Report the malaria status.
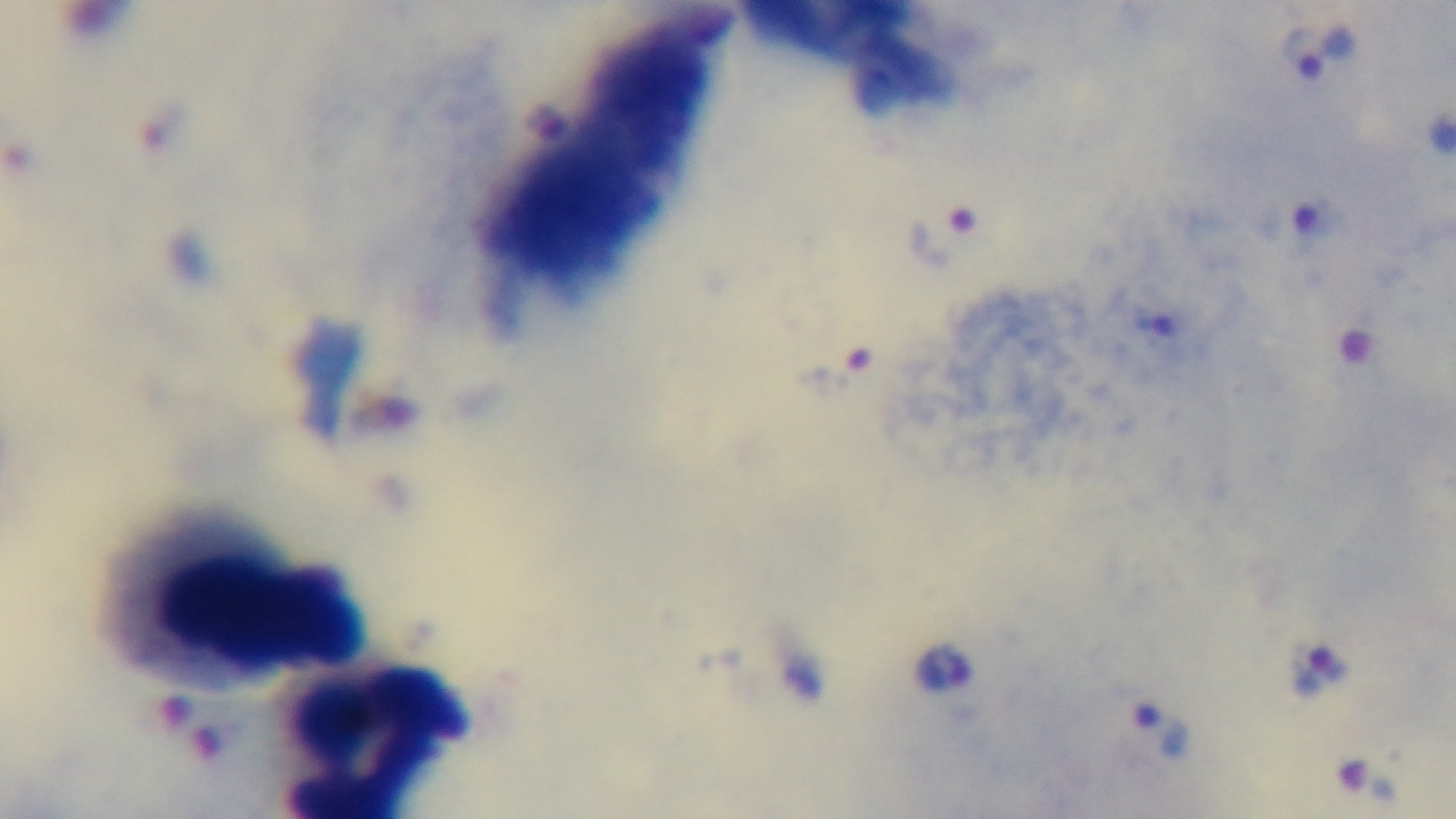
It is infected.

Single field of view. Photomicrograph. Oil-immersion objective, 100x. Mounted 4K digital camera. Giemsa stain. Preparation: thick.